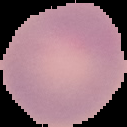

Summary:
  - Result: no Plasmodium parasites seen
  - Preparation: thin blood smear
  - Image type: segmented cell region with the area outside set to black
  - Image size: 127×127 pixels